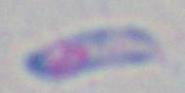
Captured at 1000x magnification. Photomicrograph. Toxoplasma gondii is shown.